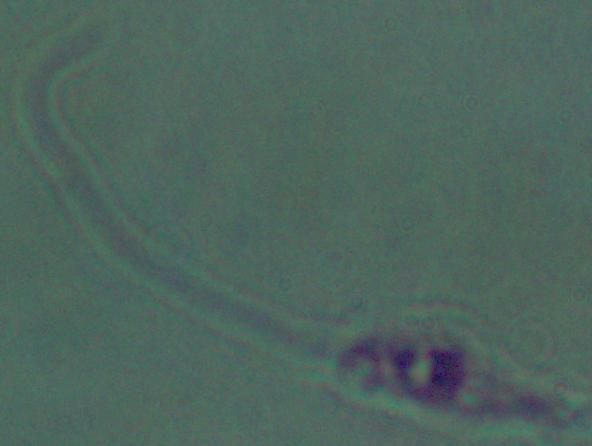
Summary:
  - Magnification: 1000x
  - Identification: Leishmania
  - Modality: micrograph